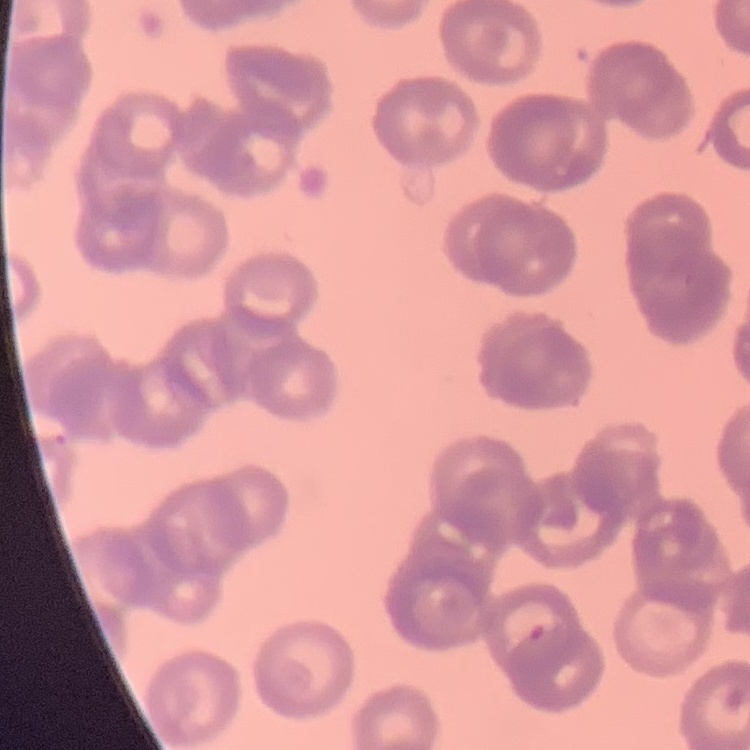

erythrocyte morphology = rouleaux formation
stain = Field's or Giemsa
image type = square crop of a larger photomicrograph
preparation = thin blood film